Evaluate for malaria.
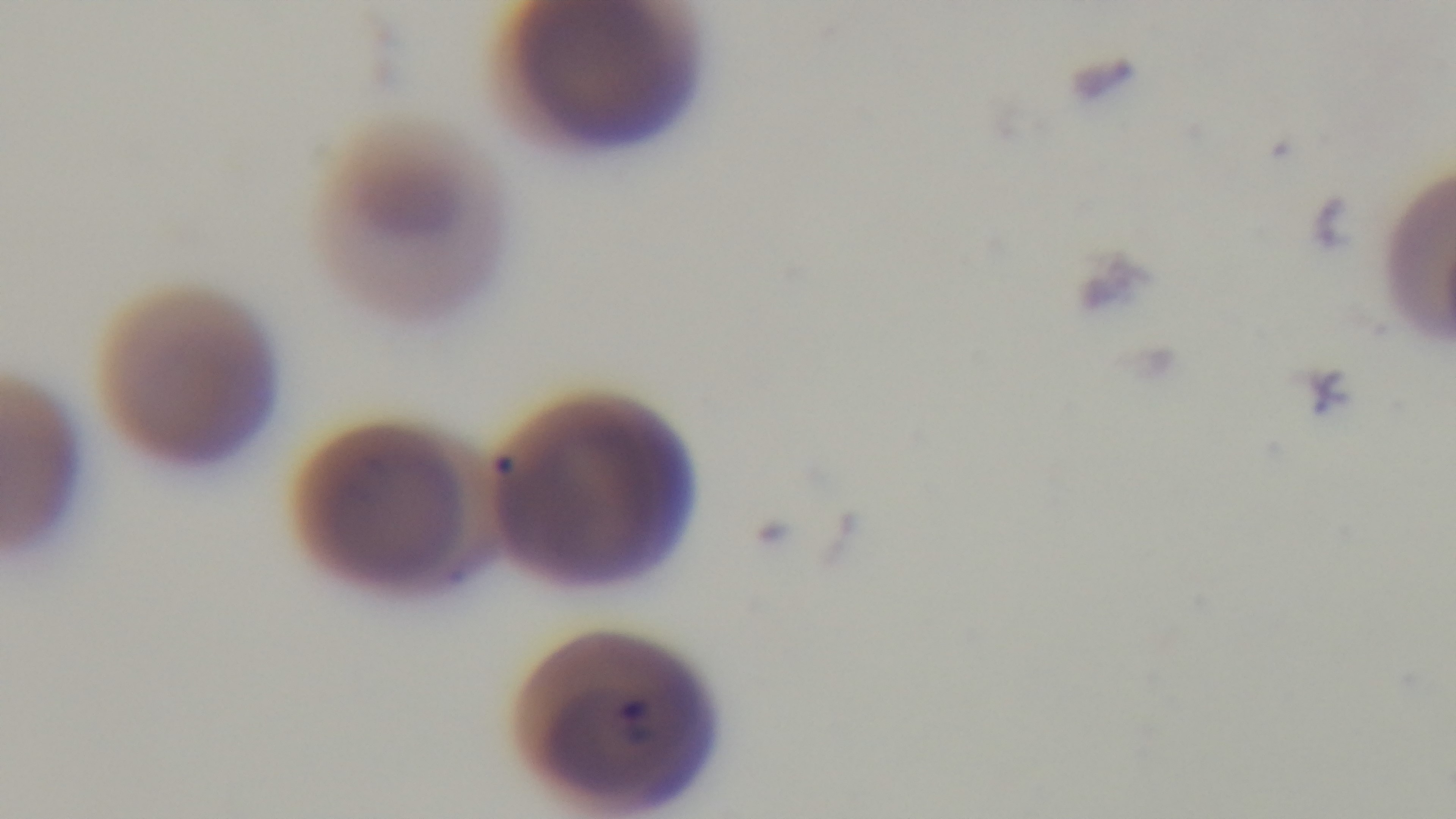

It is infected.

One field from the slide. Mounted 4K digital camera. Oil-immersion objective, 100x. Photomicrograph. Preparation: thin blood film. Giemsa-stained.